Locate every Plasmodium parasite.
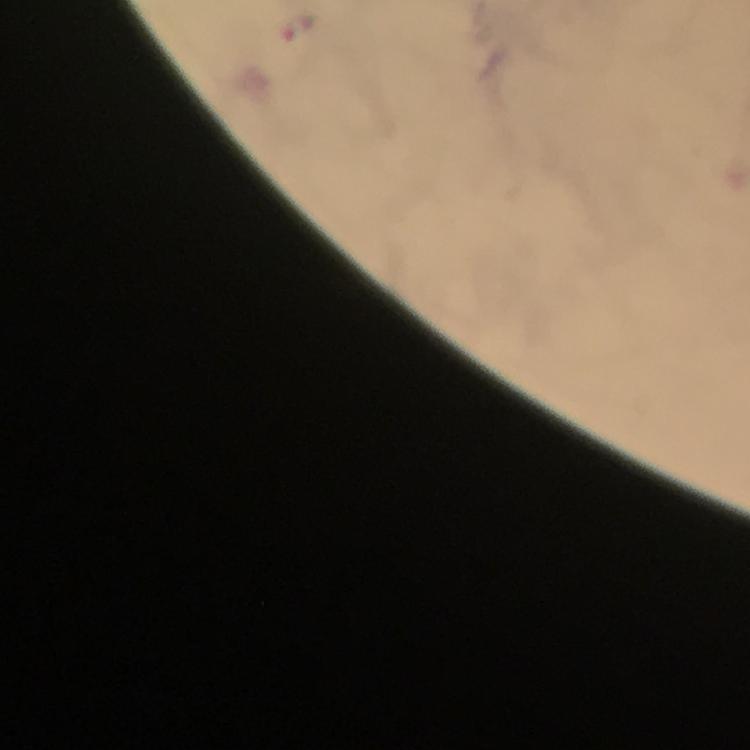
Approximate centers as [x, y] in pixels.
Plasmodium parasites: [300, 28].

Summary:
  - Stain: Giemsa
  - Immersion oil: used
  - Capture: smartphone mounted on the microscope
  - Preparation: thick smear
  - Context: from a diagnostic examination for malaria
  - Cropped from: one field of view
  - Image size: 750×750 pixels
  - Magnification: 100x